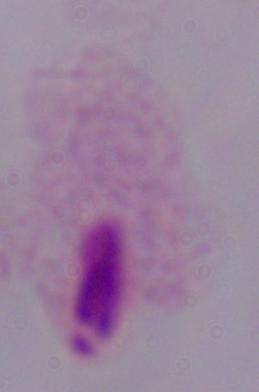
Summary:
  - Modality: photomicrograph
  - Magnification: 1000x
  - Identification: trichomonad